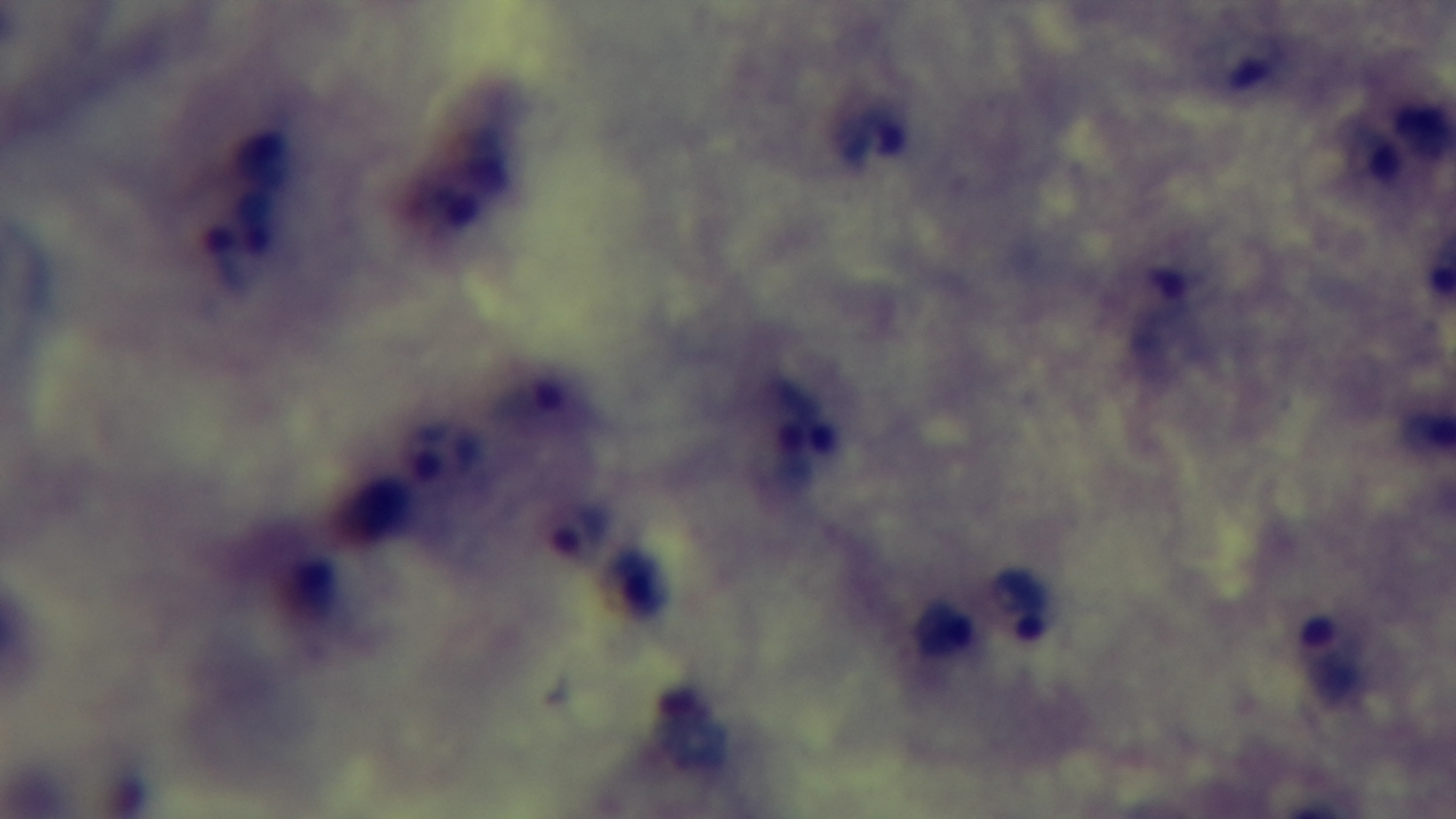

Malaria status: positive. Captured with a mounted 4K digital camera. Light microscopy. 100x oil-immersion objective. One field from the slide. Giemsa stain. Preparation: thick blood film.